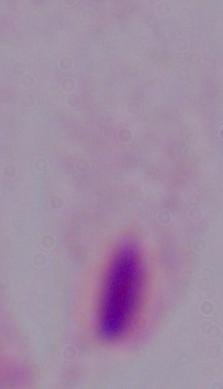

Summary:
  - Modality: micrograph
  - Magnification: 1000x
  - Identification: trichomonad